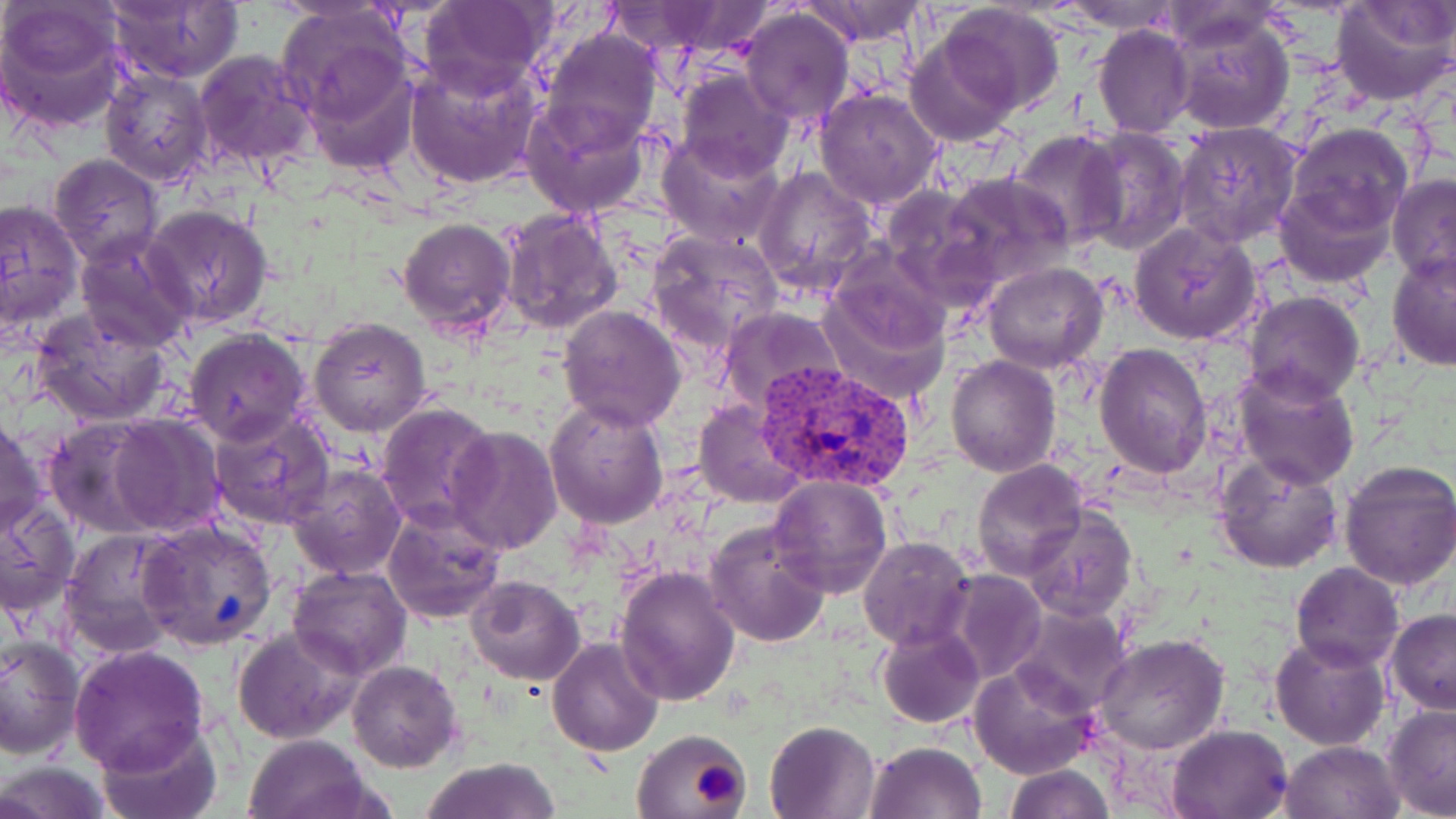
Approximate bounding boxes as (x1, y1, x2, y2) in pixels. Platelet locations: (686, 754, 745, 812). Uninfected red blood cell locations: (103, 0, 244, 84), (416, 0, 553, 102), (1328, 0, 1455, 108), (805, 1, 927, 49), (1063, 1, 1180, 34), (603, 3, 745, 56), (938, 3, 1065, 115), (0, 4, 128, 135), (739, 8, 855, 127), (281, 9, 417, 154), (1167, 13, 1295, 135), (1091, 24, 1197, 137), (539, 27, 662, 153), (904, 33, 1020, 148), (192, 47, 319, 173), (405, 58, 543, 190), (675, 66, 794, 180), (99, 69, 212, 187), (814, 87, 945, 210), (520, 95, 650, 220), (1173, 120, 1303, 249), (1287, 122, 1415, 235), (1076, 126, 1192, 255), (1010, 130, 1128, 250), (655, 133, 786, 247), (48, 156, 164, 268), (753, 165, 877, 298), (941, 172, 1073, 286), (1388, 174, 1456, 287), (1273, 181, 1393, 286), (878, 184, 997, 301), (0, 198, 84, 335), (142, 204, 273, 330), (498, 208, 622, 335), (397, 216, 518, 339), (1128, 222, 1262, 345), (648, 228, 783, 354), (75, 231, 198, 353), (1386, 250, 1456, 372), (983, 262, 1109, 373), (815, 281, 951, 405), (1243, 291, 1364, 406), (557, 304, 687, 433), (716, 306, 845, 417), (32, 307, 171, 425), (309, 316, 432, 435), (182, 329, 311, 448), (1094, 344, 1212, 480), (947, 354, 1061, 476), (1233, 366, 1361, 490), (696, 399, 805, 507), (544, 400, 669, 529), (375, 401, 498, 531), (205, 408, 336, 531), (105, 414, 225, 537), (43, 416, 167, 538), (0, 418, 47, 539), (447, 426, 562, 554), (1213, 452, 1345, 574), (1335, 459, 1456, 590), (972, 461, 1089, 580), (286, 462, 407, 580), (766, 471, 893, 597), (0, 500, 78, 617), (381, 504, 506, 625), (1023, 508, 1138, 622), (704, 520, 833, 648), (138, 521, 276, 650), (59, 527, 186, 657), (858, 537, 975, 651), (1290, 562, 1403, 673), (287, 564, 413, 679), (615, 565, 742, 706), (945, 570, 1047, 683), (466, 575, 585, 686), (1009, 604, 1132, 717), (1386, 610, 1456, 714), (877, 625, 984, 729), (233, 626, 362, 745), (1270, 634, 1391, 750), (0, 635, 83, 760), (1094, 635, 1228, 756), (547, 636, 663, 756), (67, 643, 210, 775), (347, 660, 462, 772), (970, 661, 1095, 779), (1382, 704, 1456, 817), (96, 720, 220, 819), (764, 720, 881, 819), (1166, 724, 1292, 818), (631, 728, 751, 818), (243, 734, 374, 819), (1280, 740, 1403, 818), (865, 741, 985, 819), (421, 757, 561, 819), (1, 759, 111, 819), (1003, 764, 1115, 818). Plasmodium vivax-infected red blood cell locations: (753, 359, 918, 495). Slide-level diagnosis: Plasmodium vivax. Captured at 1000x magnification. Thin blood film. Optical microscopy. May-Grünwald-Giemsa stain. Single field of view. Image is 1456×819 pixels.